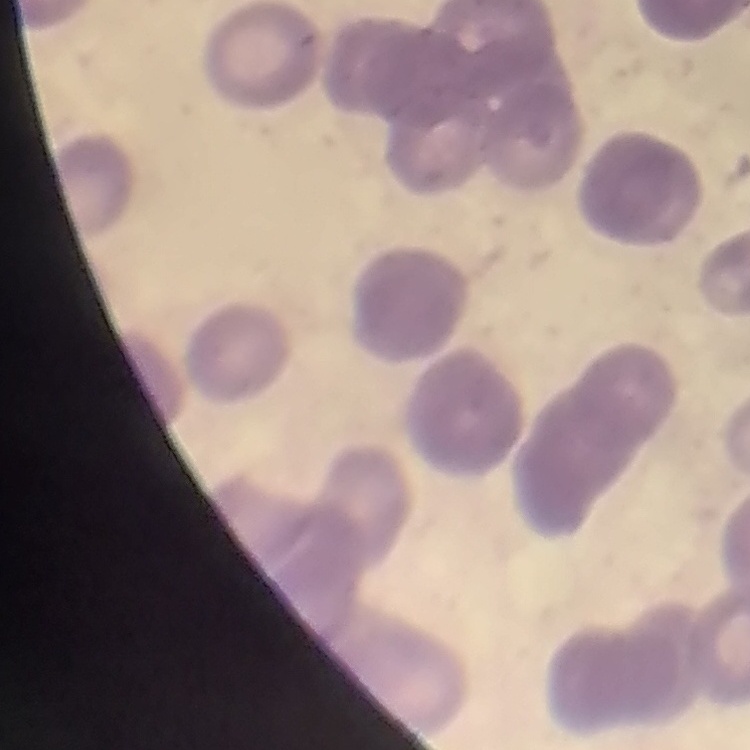
{
  "erythrocyte_morphology": "rouleaux formation",
  "preparation": "thin blood smear",
  "stain": "Field's or Giemsa",
  "image_type": "square crop of a larger photomicrograph"
}